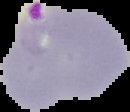

Summary:
  - Preparation: thin blood smear
  - Result: malaria parasites identified
  - Image type: segmented cell region with the area outside set to black
  - Image size: 130×112 pixels